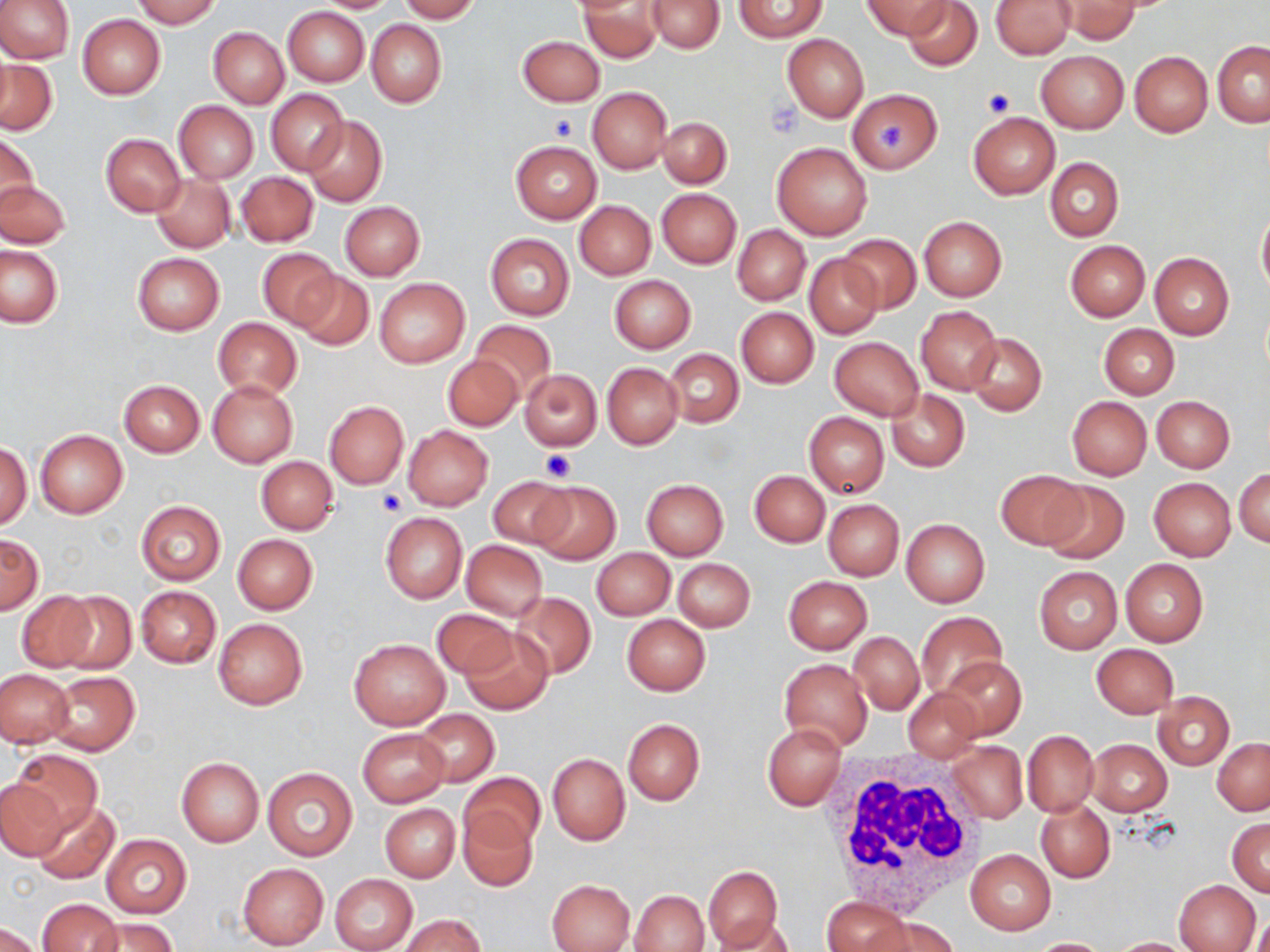
Summary:
  - Coordinate format: approximate bounding boxes as (x1, y1, x2, y2) in pixels
  - White blood cell locations: (824, 751, 988, 916)
  - Uninfected red blood cell locations: (0, 0, 73, 64), (133, 0, 221, 28), (312, 0, 401, 12), (397, 0, 481, 22), (648, 0, 725, 52), (862, 0, 949, 39), (902, 0, 981, 71), (1057, 0, 1140, 43), (734, 1, 825, 43), (990, 1, 1075, 59), (580, 2, 663, 62), (283, 6, 369, 86), (77, 14, 165, 99), (367, 19, 446, 109), (208, 27, 288, 108), (782, 34, 869, 121), (517, 35, 604, 106), (1212, 41, 1270, 127), (1036, 50, 1128, 134), (1129, 51, 1212, 136), (0, 61, 58, 135), (587, 87, 672, 174), (266, 88, 347, 175), (847, 90, 941, 172), (173, 101, 259, 183), (968, 111, 1060, 199), (658, 117, 732, 188), (305, 118, 387, 205), (1, 132, 38, 212), (101, 133, 185, 216), (510, 141, 601, 223), (772, 142, 872, 240), (1045, 157, 1123, 241), (1055, 159, 1133, 322), (236, 171, 318, 247), (150, 173, 235, 253), (0, 179, 71, 248), (657, 188, 741, 269), (340, 201, 424, 280), (575, 201, 656, 280), (1257, 207, 1270, 299), (919, 216, 1007, 300), (732, 225, 811, 305), (840, 229, 1003, 308), (485, 233, 574, 320), (838, 234, 920, 313), (1065, 241, 1150, 321), (1, 246, 63, 327), (258, 247, 337, 329), (131, 252, 224, 335), (1149, 252, 1234, 340), (804, 254, 883, 339), (292, 271, 373, 350), (610, 275, 696, 352), (374, 276, 470, 368), (916, 306, 1001, 393), (736, 307, 819, 387), (212, 317, 302, 400), (470, 321, 556, 401), (1100, 324, 1179, 398), (964, 333, 1047, 417), (830, 337, 923, 420), (663, 348, 744, 427), (442, 353, 522, 431), (602, 363, 682, 449), (517, 368, 602, 451), (118, 379, 204, 456), (208, 379, 298, 467), (886, 389, 969, 472), (1151, 396, 1234, 473), (1066, 397, 1151, 480), (324, 401, 408, 488), (803, 412, 888, 498), (403, 425, 493, 510), (35, 429, 128, 518), (1, 441, 31, 530), (256, 456, 338, 535), (995, 469, 1087, 548), (1235, 469, 1269, 549), (750, 471, 829, 546), (486, 475, 573, 549), (1148, 477, 1236, 560), (641, 479, 729, 559), (1040, 480, 1129, 565), (530, 481, 620, 565), (823, 499, 903, 579), (135, 501, 225, 584), (380, 513, 467, 603), (901, 518, 990, 607), (232, 534, 317, 613), (0, 535, 42, 615), (460, 540, 548, 620), (593, 549, 675, 620), (672, 558, 756, 631), (1120, 558, 1207, 647), (1033, 565, 1122, 654), (783, 576, 872, 654), (136, 586, 221, 668), (55, 591, 136, 675), (16, 592, 99, 673), (511, 592, 597, 679), (432, 608, 516, 678), (916, 612, 1006, 699), (622, 615, 710, 695), (213, 618, 307, 709), (459, 630, 553, 715), (849, 631, 924, 715), (349, 638, 449, 729), (1092, 644, 1178, 718), (939, 656, 1026, 739), (780, 658, 872, 752), (1, 670, 73, 747), (47, 671, 139, 755), (902, 688, 985, 760), (1154, 691, 1234, 768), (415, 709, 498, 787), (622, 718, 704, 806), (763, 722, 846, 810), (357, 728, 449, 806), (1022, 730, 1098, 817), (1213, 737, 1270, 815), (1089, 739, 1172, 816), (948, 741, 1027, 823), (9, 749, 103, 835), (547, 752, 630, 845), (176, 757, 264, 847), (263, 767, 358, 861), (460, 772, 545, 850), (0, 780, 69, 860), (32, 799, 121, 884), (1036, 800, 1114, 882), (380, 804, 460, 882), (459, 808, 537, 891), (1227, 818, 1270, 895), (100, 835, 190, 918), (966, 850, 1055, 934), (238, 863, 327, 948), (702, 865, 782, 950), (329, 873, 419, 952), (547, 878, 634, 952), (1173, 878, 1260, 952), (630, 889, 709, 951), (823, 897, 912, 951), (36, 898, 123, 952), (1249, 914, 1270, 952), (400, 915, 485, 952), (89, 916, 176, 952), (712, 916, 799, 951), (869, 916, 959, 952), (0, 923, 42, 952), (1109, 937, 1197, 951), (1026, 938, 1115, 952)
  - Platelet locations: (981, 88, 1015, 117), (767, 97, 801, 137), (550, 114, 578, 141), (880, 125, 906, 154), (539, 449, 577, 480), (378, 490, 408, 516)
  - Slide-level diagnosis: no evidence of blood parasites
  - Preparation: thin blood smear
  - Magnification: 1000x
  - Stain: May-Grünwald-Giemsa
  - Field of view: single
  - Image size: 1270×952 pixels
  - Modality: light microscopy